Name the parasite shown.
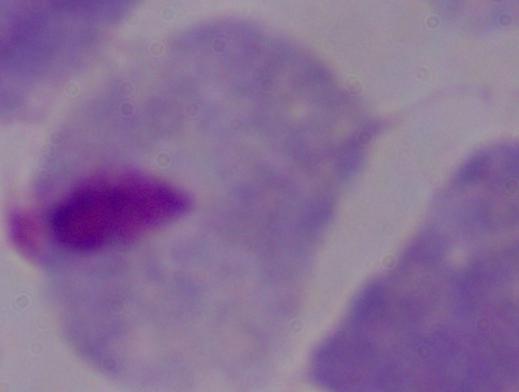

This is a trichomonad.

Summary:
  - Modality: photomicrograph
  - Magnification: 1000x